Locate and identify every blood parasite.
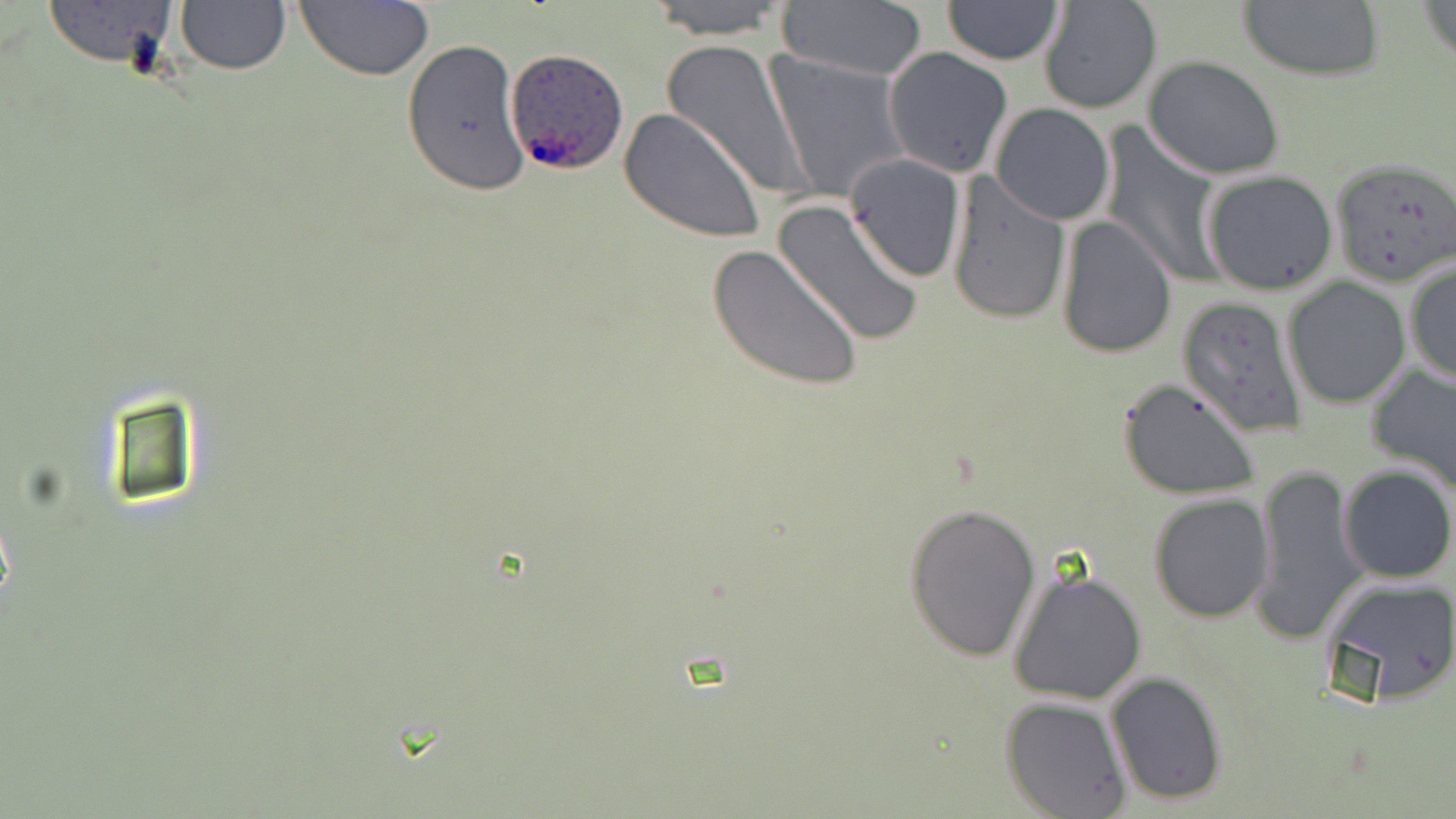

Approximate bounding boxes as named x1/y1/x2/y2 corners in pixels.
Plasmodium ovale-infected red blood cells: (x1=504, y1=48, x2=630, y2=176).
No Plasmodium falciparum, Plasmodium malariae, Plasmodium vivax, Babesia divergens, or Trypanosoma brucei observed.

Summary:
  - Uninfected red blood cell locations: (x1=40, y1=0, x2=183, y2=70), (x1=638, y1=0, x2=796, y2=40), (x1=942, y1=0, x2=1063, y2=64), (x1=1234, y1=0, x2=1388, y2=81), (x1=1422, y1=0, x2=1455, y2=67), (x1=293, y1=1, x2=436, y2=81), (x1=1038, y1=1, x2=1162, y2=115), (x1=174, y1=2, x2=290, y2=75), (x1=775, y1=2, x2=929, y2=81), (x1=657, y1=37, x2=812, y2=203), (x1=403, y1=38, x2=530, y2=197), (x1=883, y1=47, x2=1013, y2=176), (x1=764, y1=51, x2=912, y2=203), (x1=1143, y1=55, x2=1285, y2=179), (x1=990, y1=104, x2=1115, y2=224), (x1=619, y1=109, x2=766, y2=242), (x1=1097, y1=124, x2=1227, y2=287), (x1=845, y1=153, x2=967, y2=284), (x1=1330, y1=157, x2=1456, y2=286), (x1=1201, y1=170, x2=1339, y2=296), (x1=944, y1=172, x2=1072, y2=326), (x1=772, y1=199, x2=925, y2=345), (x1=1055, y1=216, x2=1179, y2=359), (x1=708, y1=245, x2=866, y2=393), (x1=1404, y1=260, x2=1455, y2=387), (x1=1282, y1=278, x2=1410, y2=408), (x1=1178, y1=297, x2=1308, y2=436), (x1=1364, y1=363, x2=1456, y2=497), (x1=1116, y1=377, x2=1263, y2=502), (x1=1252, y1=464, x2=1367, y2=643), (x1=1337, y1=465, x2=1455, y2=583), (x1=1148, y1=493, x2=1274, y2=623), (x1=903, y1=501, x2=1041, y2=661), (x1=1008, y1=569, x2=1149, y2=705), (x1=1317, y1=572, x2=1456, y2=705), (x1=1104, y1=671, x2=1230, y2=806), (x1=1001, y1=696, x2=1131, y2=817)
  - Slide-level diagnosis: Plasmodium ovale
  - Image size: 1456×819 pixels
  - Field of view: one of a larger specimen
  - Stain: May-Grünwald-Giemsa
  - Magnification: 1000x
  - Preparation: thin blood smear
  - Modality: optical microscopy